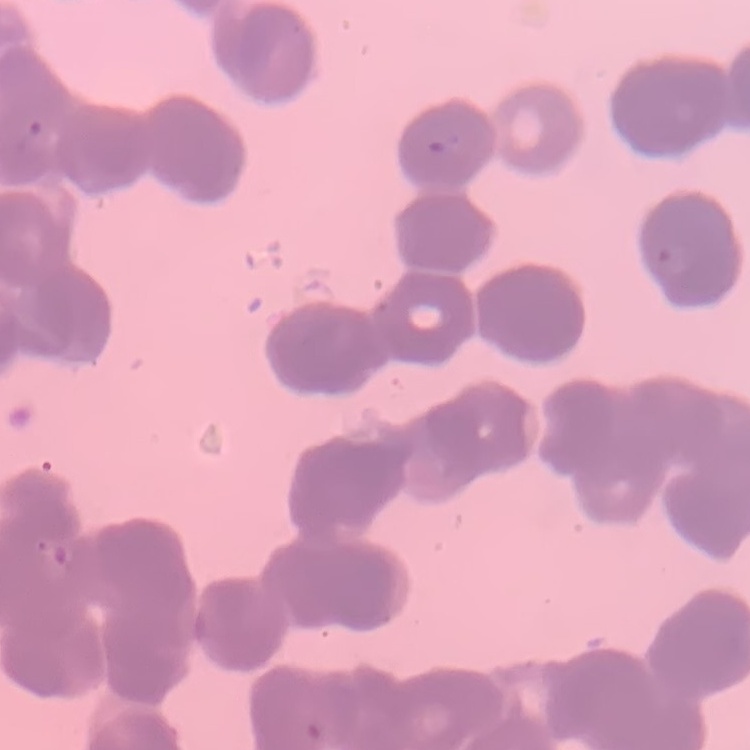

Summary:
  - Erythrocyte morphology: rouleaux formation
  - Stain: Field's or Giemsa
  - Preparation: thin peripheral smear
  - Image type: one tile cut from a larger photomicrograph